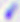
Captured at 400x magnification. Photomicrograph. Toxoplasma gondii is seen.